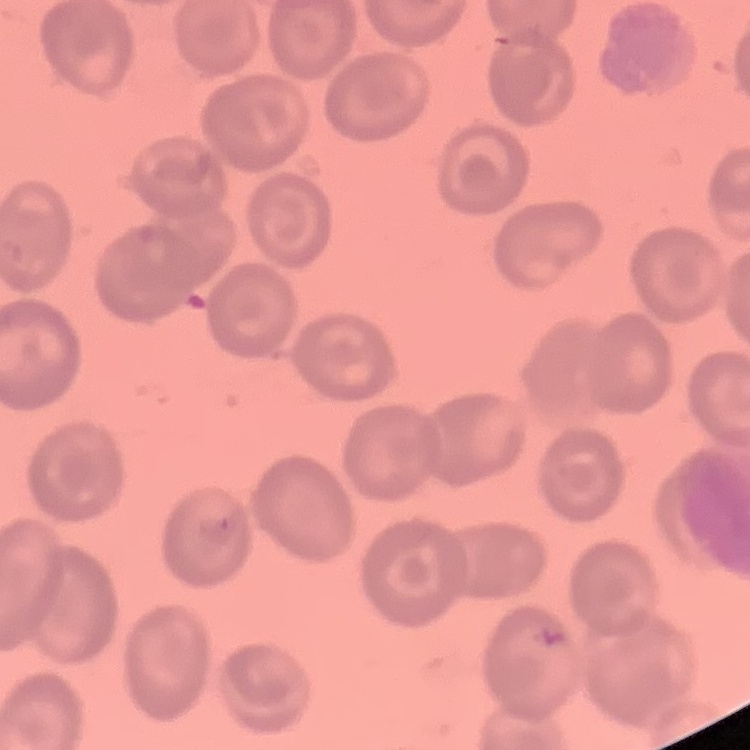

Summary:
  - Erythrocyte morphology: no rouleaux formation
  - Image type: square crop of a larger photomicrograph
  - Preparation: thin peripheral smear
  - Stain: Field's or Giemsa